Locate every blood parasite and identify its species.
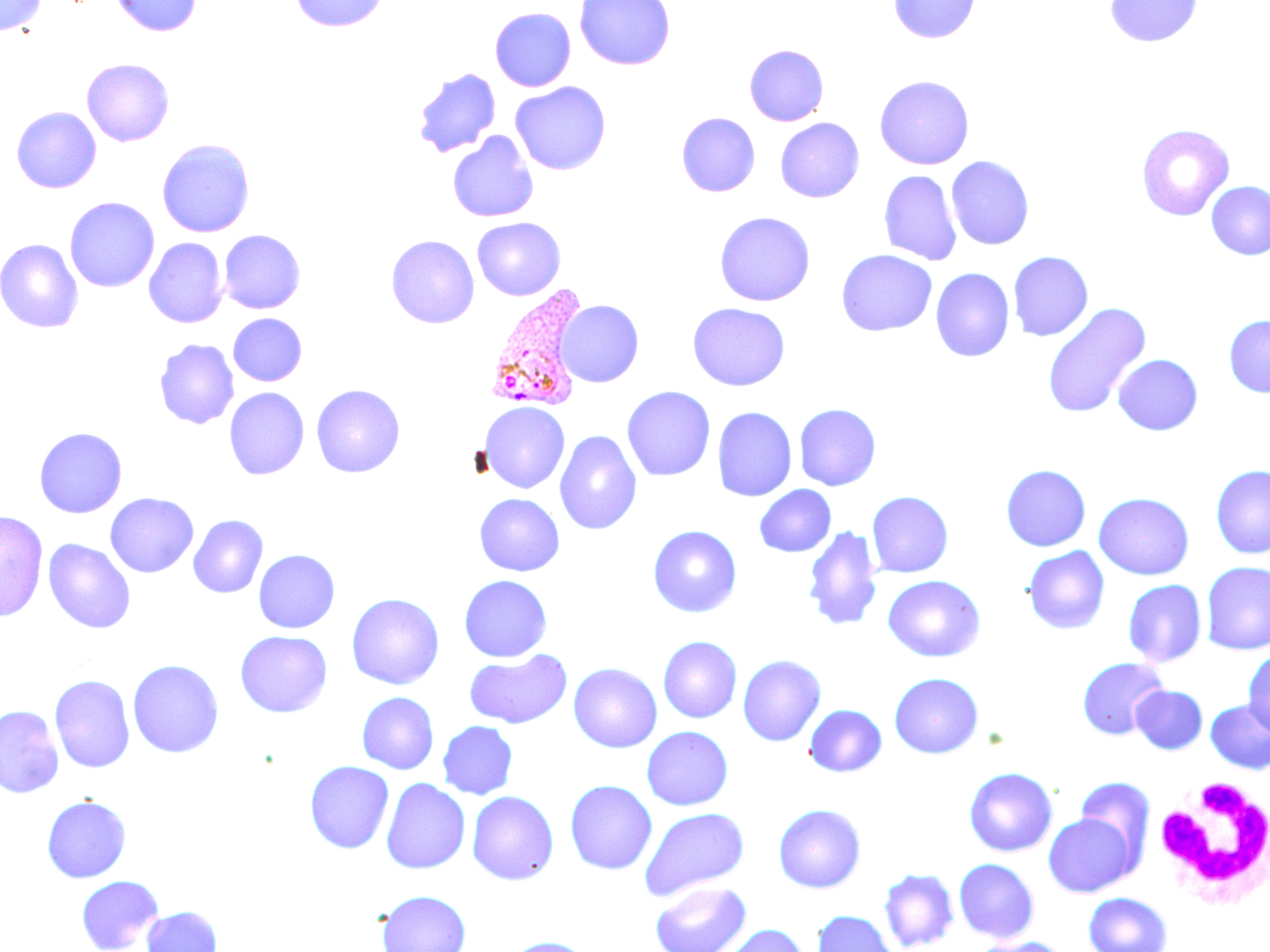
Approximate bounding boxes as (x1, y1, x2, y2) in pixels.
Plasmodium vivax-infected red blood cells: (485, 285, 590, 412).
No Plasmodium falciparum, Plasmodium ovale, Plasmodium malariae, Babesia divergens, or Trypanosoma brucei observed.

Summary:
  - White blood cell locations: (1151, 778, 1270, 912)
  - Uninfected red blood cell locations: (0, 0, 46, 37), (110, 0, 202, 37), (289, 0, 389, 32), (574, 0, 675, 70), (888, 0, 980, 43), (1104, 0, 1203, 47), (490, 7, 576, 92), (744, 44, 829, 126), (82, 58, 174, 147), (412, 68, 501, 158), (874, 75, 974, 170), (510, 81, 611, 175), (11, 106, 102, 193), (677, 112, 760, 197), (775, 117, 865, 202), (1136, 123, 1234, 221), (447, 131, 538, 222), (156, 138, 255, 238), (946, 156, 1034, 250), (878, 170, 962, 266), (1206, 181, 1270, 260), (64, 196, 160, 292), (715, 211, 815, 306), (472, 217, 565, 301), (219, 230, 305, 314), (386, 234, 480, 328), (144, 237, 228, 328), (0, 238, 84, 333), (836, 249, 937, 336), (1008, 251, 1093, 341), (931, 268, 1015, 362), (556, 299, 644, 387), (687, 303, 790, 390), (1041, 303, 1151, 418), (228, 313, 307, 386), (1224, 314, 1270, 398), (153, 338, 239, 430), (1113, 354, 1203, 435), (311, 384, 406, 478), (622, 385, 715, 481), (224, 387, 310, 480), (480, 401, 569, 493), (794, 403, 881, 490), (712, 407, 797, 502), (34, 427, 127, 518), (554, 430, 642, 535), (1001, 464, 1091, 551), (1211, 464, 1270, 559), (754, 484, 836, 558), (866, 491, 954, 578), (105, 492, 199, 577), (1093, 492, 1195, 580), (474, 493, 564, 576), (0, 510, 48, 622), (188, 515, 268, 598), (648, 524, 742, 617), (802, 525, 882, 632), (43, 538, 136, 634), (1023, 546, 1110, 634), (253, 549, 340, 633), (1200, 561, 1270, 655), (459, 575, 552, 662), (883, 575, 985, 662), (1122, 579, 1206, 667), (346, 593, 445, 690), (234, 630, 332, 717), (658, 636, 742, 723), (464, 649, 572, 729), (1243, 649, 1270, 736), (737, 654, 826, 746), (1076, 656, 1169, 740), (127, 659, 224, 758), (568, 663, 662, 753), (889, 672, 984, 758), (49, 674, 135, 773), (1131, 685, 1208, 754), (356, 692, 439, 774), (1205, 699, 1270, 775), (804, 704, 887, 777), (0, 705, 65, 799), (437, 721, 518, 799), (641, 726, 733, 810), (304, 760, 394, 854), (963, 766, 1058, 856), (1073, 776, 1156, 872), (381, 778, 471, 874), (565, 779, 657, 874), (466, 790, 559, 885), (41, 795, 131, 883), (773, 803, 866, 893), (638, 807, 749, 901), (1044, 812, 1136, 897), (954, 858, 1039, 943), (878, 868, 959, 951), (76, 875, 164, 952), (650, 881, 751, 952), (376, 890, 471, 952), (1083, 892, 1173, 952), (142, 906, 222, 952), (813, 910, 900, 952), (715, 924, 808, 952), (504, 936, 592, 952), (971, 936, 1068, 952)
  - Slide-level diagnosis: Plasmodium vivax
  - Field of view: one of a larger specimen
  - Magnification: 1000x
  - Preparation: thin blood film
  - Stain: May-Grünwald-Giemsa
  - Modality: optical microscopy
  - Image size: 1270×952 pixels